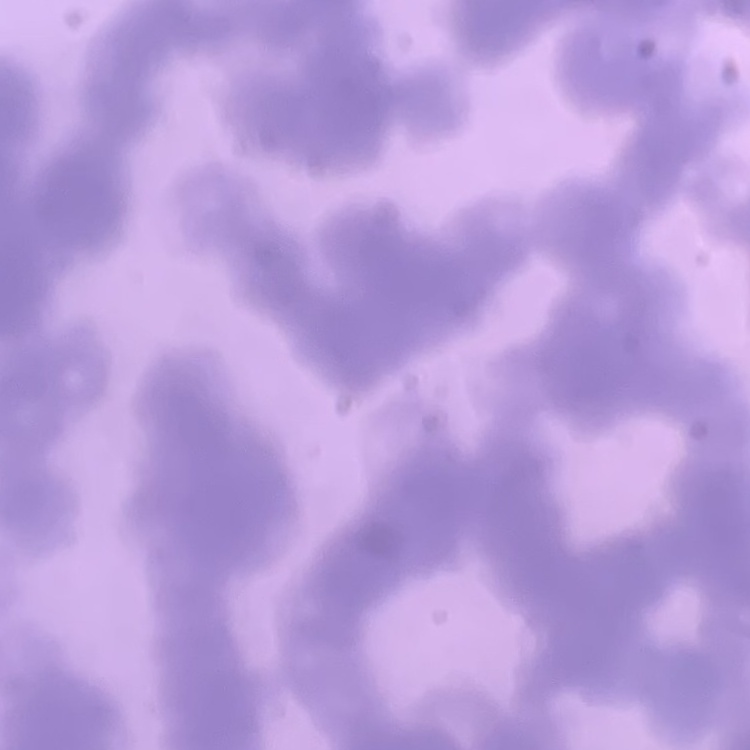
The red blood cells exhibit rouleaux formation. Thin peripheral smear. One tile cut from a larger photomicrograph. Field's or Giemsa stain.